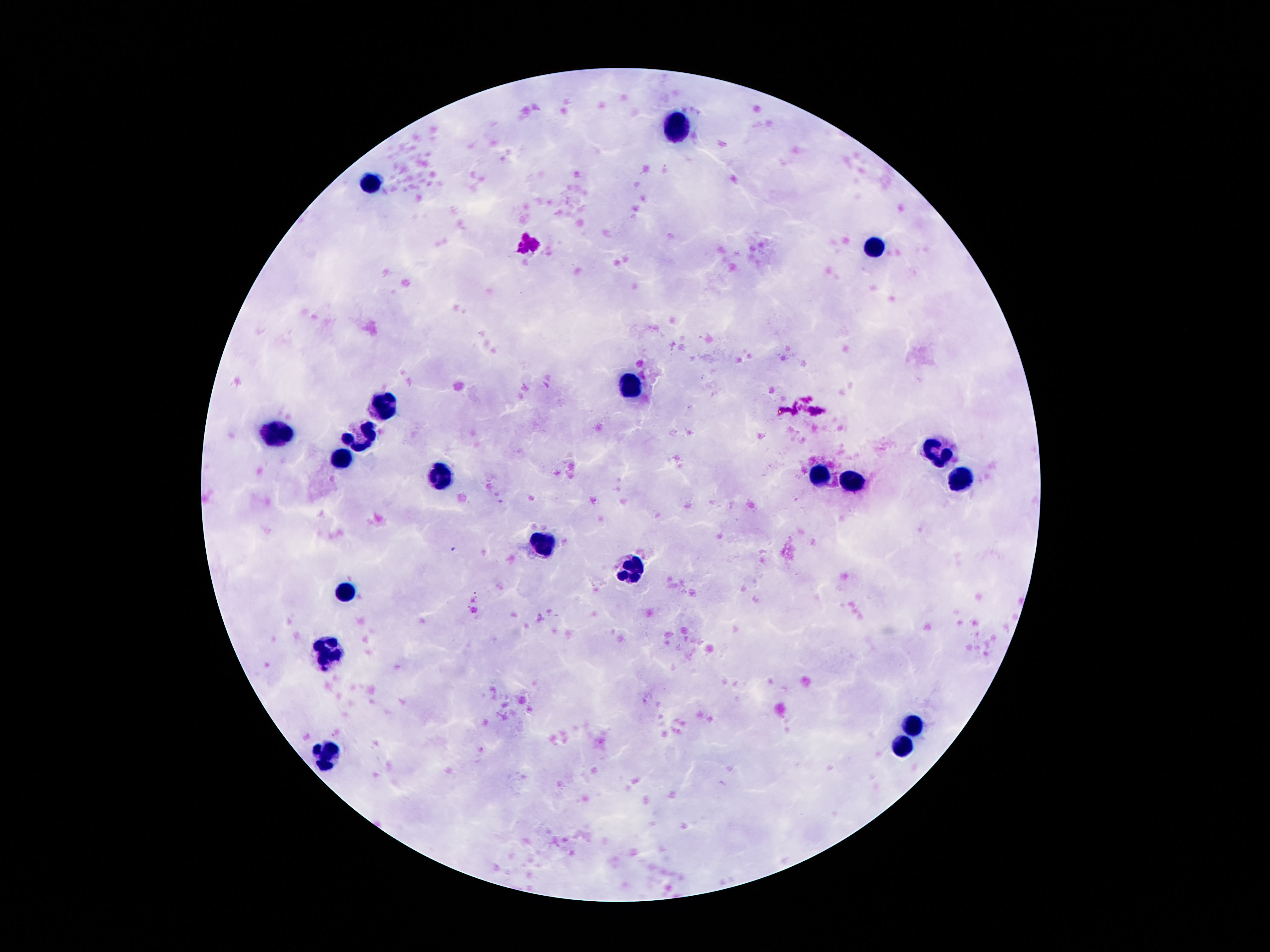

Approximate object centers, in pixels from the top-left corner. Leukocyte locations: (x=678, y=127), (x=371, y=186), (x=874, y=247), (x=629, y=386), (x=385, y=405), (x=278, y=430), (x=360, y=434), (x=934, y=453), (x=342, y=460), (x=440, y=477), (x=819, y=477), (x=962, y=479), (x=850, y=483), (x=543, y=543), (x=631, y=569), (x=350, y=591), (x=328, y=654), (x=913, y=724), (x=899, y=746), (x=328, y=753). Giemsa stain. Photographed through the microscope eyepiece with a smartphone camera. 100x magnification. Image is 1270×952 pixels. Patient malaria status: not infected. Single field of view. Thick blood smear.